Locate every Plasmodium parasite.
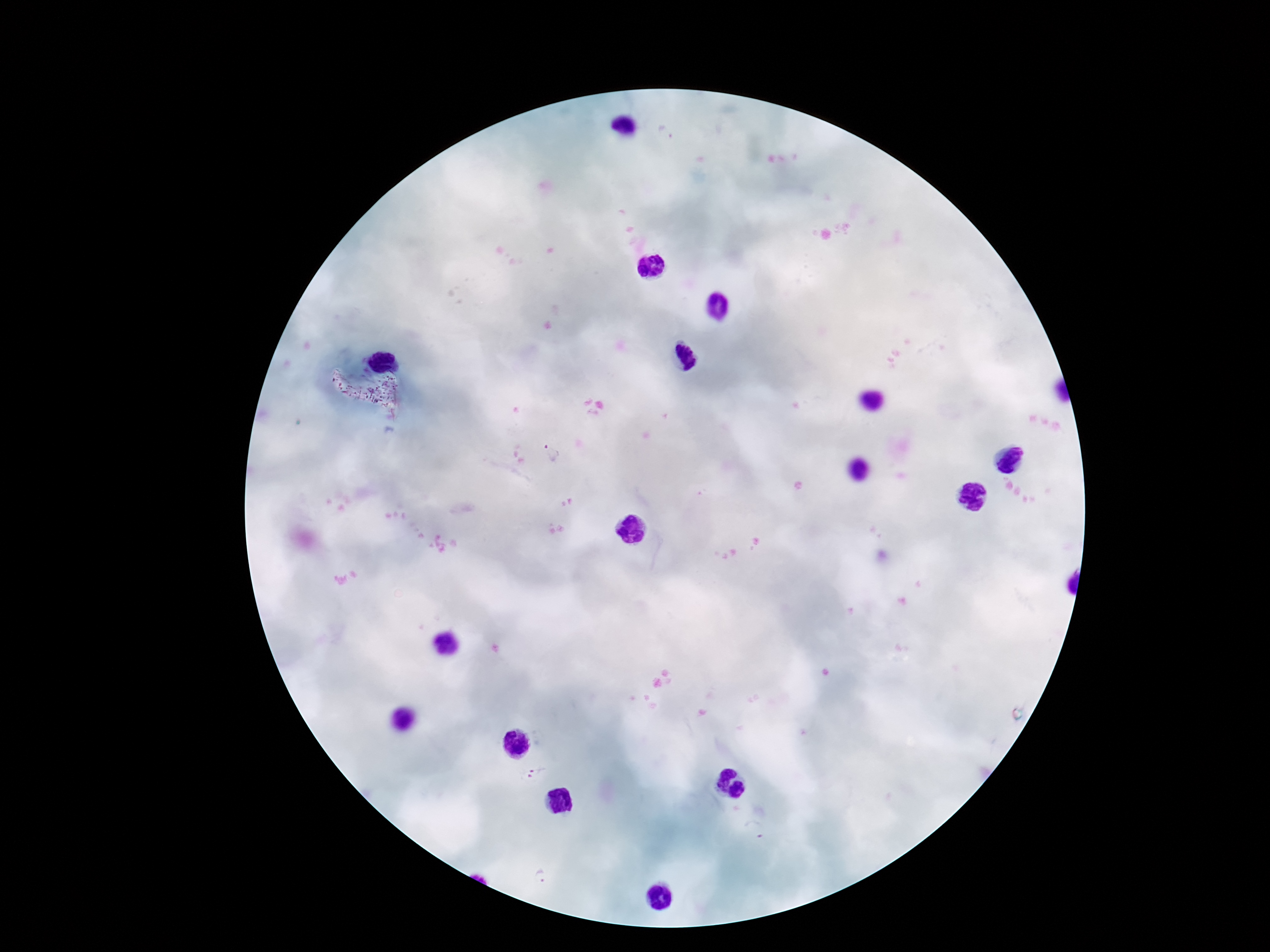

Approximate centers as [x, y] in pixels.
Plasmodium parasites: [665, 133], [552, 452], [537, 774].

Giemsa-stained preparation. 100x magnification. Thick peripheral-blood smear. Smartphone photograph taken through the microscope eyepiece. One field from this slide. Patient malaria status: infected. Image is 1270×952 pixels.